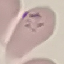

Result: no malaria parasites seen. Acquired by smartphone through the microscope eyepiece. Thin smear of blood. Cell patch, automatically extracted from a larger field of view and resized to 64 × 64 pixels. Giemsa-stained preparation.